Classify this cell by malaria status.
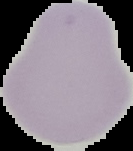
Uninfected.

image size = 133×151 pixels
image type = segmented cell region on a black background
preparation = thin blood smear